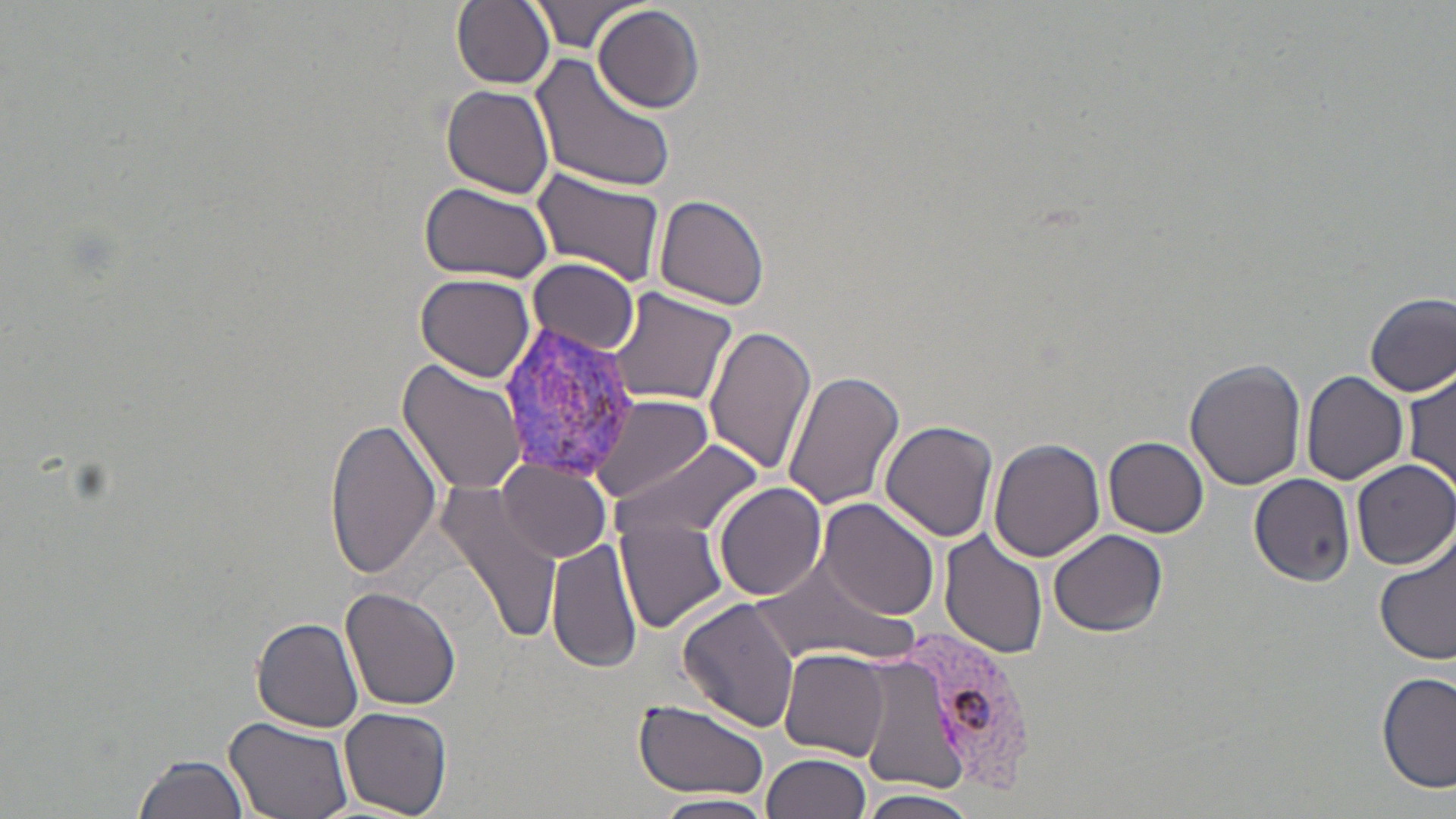
slide-level diagnosis = Plasmodium vivax
modality = optical microscopy
image size = 1456×819 pixels
uninfected red blood cell locations = approximate bounding boxes as (x1, y1, x2, y2) in pixels: (451, 0, 555, 89), (532, 0, 642, 54), (593, 4, 705, 114), (529, 54, 677, 195), (442, 85, 556, 199), (531, 167, 668, 289), (419, 183, 554, 283), (655, 194, 772, 310), (528, 258, 640, 353), (420, 267, 646, 363), (415, 273, 536, 383), (608, 287, 741, 407), (1365, 293, 1456, 397), (701, 323, 817, 474), (1184, 357, 1307, 489), (398, 362, 527, 496), (1406, 366, 1454, 495), (781, 368, 909, 513), (1300, 370, 1408, 487), (586, 394, 714, 504), (325, 418, 443, 579), (879, 421, 998, 542), (1104, 436, 1208, 537), (990, 438, 1104, 562), (613, 440, 765, 544), (1349, 458, 1456, 570), (501, 460, 614, 564), (1248, 473, 1354, 583), (431, 481, 563, 643), (714, 482, 829, 601), (819, 499, 941, 621), (614, 514, 734, 635), (1047, 528, 1167, 637), (938, 533, 1050, 662), (546, 534, 642, 677), (1374, 540, 1456, 666), (752, 556, 915, 668), (340, 587, 461, 713), (676, 597, 801, 735), (251, 616, 366, 732), (862, 628, 970, 801), (778, 648, 891, 762), (1376, 673, 1454, 792), (633, 698, 771, 803), (339, 707, 452, 818), (222, 715, 354, 819), (133, 751, 251, 819), (760, 752, 869, 819), (859, 789, 977, 819), (653, 793, 776, 819)
magnification = 1000x
preparation = thin blood film
field of view = single
Plasmodium vivax-infected red blood cell locations = approximate bounding boxes as (x1, y1, x2, y2) in pixels: (505, 322, 642, 483), (906, 623, 1049, 799)
stain = May-Grünwald-Giemsa